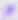
modality = micrograph
magnification = 400x
identification = Toxoplasma gondii